Identify the blood parasite species.
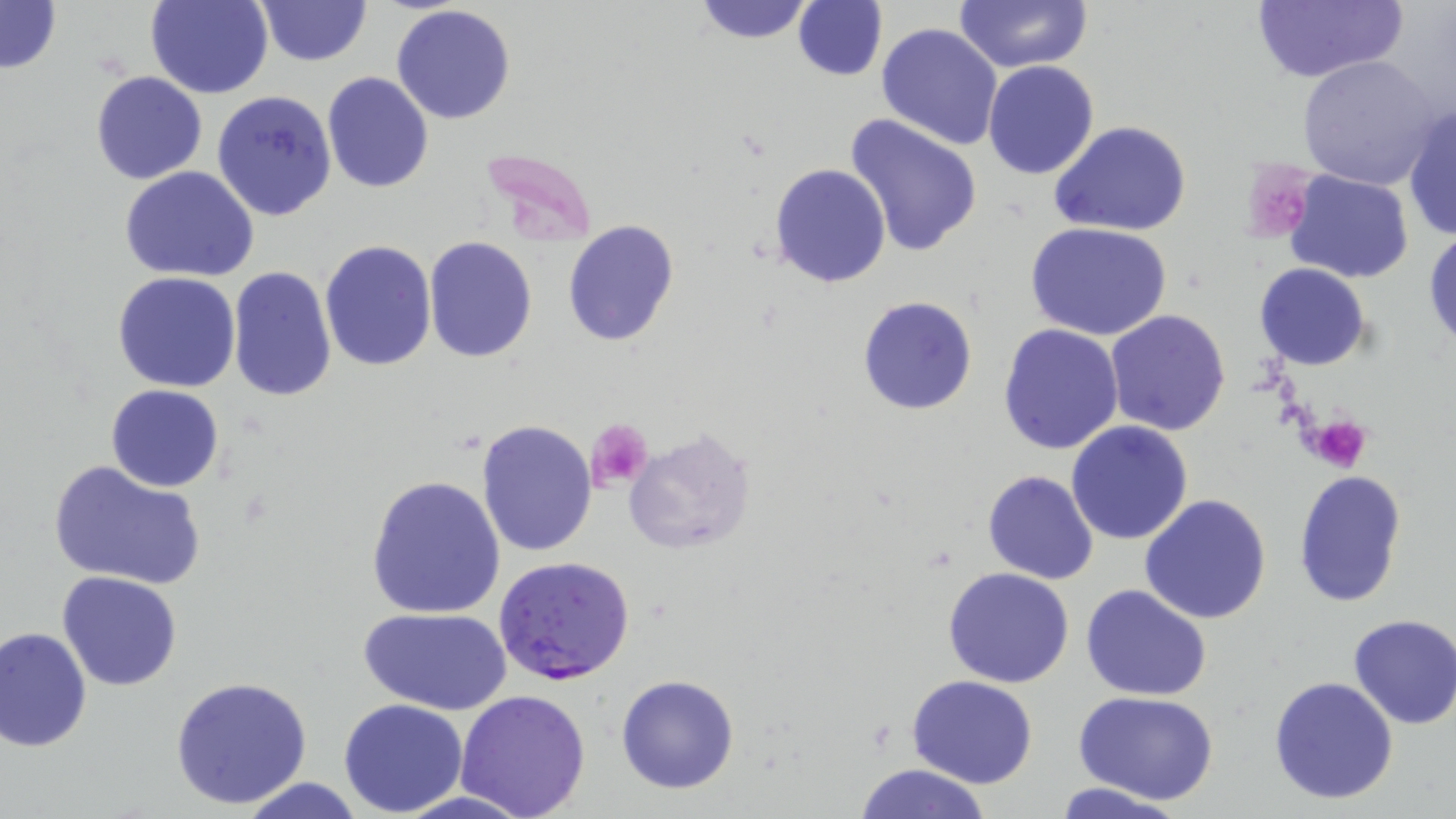

Plasmodium falciparum.

Summary:
  - Coordinate format: approximate bounding boxes as named x1/y1/x2/y2 corners in pixels
  - Uninfected red blood cell locations: (x1=145, y1=0, x2=273, y2=99), (x1=256, y1=0, x2=371, y2=66), (x1=792, y1=0, x2=887, y2=82), (x1=953, y1=0, x2=1094, y2=72), (x1=0, y1=1, x2=62, y2=74), (x1=690, y1=1, x2=819, y2=45), (x1=1249, y1=1, x2=1408, y2=85), (x1=391, y1=4, x2=517, y2=125), (x1=876, y1=23, x2=1004, y2=151), (x1=1297, y1=54, x2=1443, y2=191), (x1=982, y1=60, x2=1099, y2=180), (x1=91, y1=71, x2=207, y2=185), (x1=322, y1=73, x2=434, y2=193), (x1=211, y1=90, x2=338, y2=221), (x1=1404, y1=101, x2=1455, y2=237), (x1=843, y1=113, x2=984, y2=257), (x1=1049, y1=122, x2=1191, y2=237), (x1=770, y1=163, x2=891, y2=288), (x1=119, y1=166, x2=262, y2=280), (x1=1282, y1=169, x2=1414, y2=285), (x1=561, y1=220, x2=680, y2=347), (x1=1026, y1=222, x2=1173, y2=340), (x1=1424, y1=227, x2=1456, y2=350), (x1=424, y1=237, x2=538, y2=362), (x1=319, y1=239, x2=436, y2=371), (x1=1254, y1=262, x2=1372, y2=371), (x1=228, y1=266, x2=336, y2=401), (x1=113, y1=271, x2=240, y2=392), (x1=858, y1=296, x2=977, y2=415), (x1=1104, y1=309, x2=1231, y2=437), (x1=998, y1=324, x2=1123, y2=453), (x1=106, y1=384, x2=225, y2=492), (x1=476, y1=421, x2=597, y2=557), (x1=1065, y1=421, x2=1193, y2=546), (x1=623, y1=429, x2=756, y2=557), (x1=47, y1=458, x2=206, y2=591), (x1=1293, y1=468, x2=1408, y2=608), (x1=981, y1=470, x2=1100, y2=584), (x1=366, y1=475, x2=506, y2=618), (x1=1138, y1=494, x2=1272, y2=626), (x1=943, y1=567, x2=1075, y2=688), (x1=57, y1=571, x2=184, y2=692), (x1=1082, y1=583, x2=1212, y2=701), (x1=358, y1=605, x2=511, y2=714), (x1=1347, y1=614, x2=1455, y2=730), (x1=1, y1=627, x2=93, y2=752), (x1=168, y1=674, x2=315, y2=811), (x1=615, y1=674, x2=740, y2=794), (x1=907, y1=675, x2=1037, y2=788), (x1=1267, y1=676, x2=1398, y2=806), (x1=456, y1=687, x2=591, y2=819), (x1=1074, y1=692, x2=1217, y2=805), (x1=337, y1=698, x2=468, y2=817), (x1=854, y1=762, x2=993, y2=819), (x1=236, y1=776, x2=369, y2=818), (x1=1050, y1=782, x2=1185, y2=819)
  - Plasmodium falciparum-infected red blood cell locations: (x1=494, y1=557, x2=637, y2=684)
  - Platelet locations: (x1=1254, y1=183, x2=1306, y2=237), (x1=1307, y1=413, x2=1370, y2=471), (x1=586, y1=418, x2=655, y2=492)
  - Preparation: thin blood smear
  - Field of view: one of a larger specimen
  - Magnification: 1000x
  - Modality: light microscopy
  - Image size: 1456×819 pixels
  - Stain: May-Grünwald-Giemsa